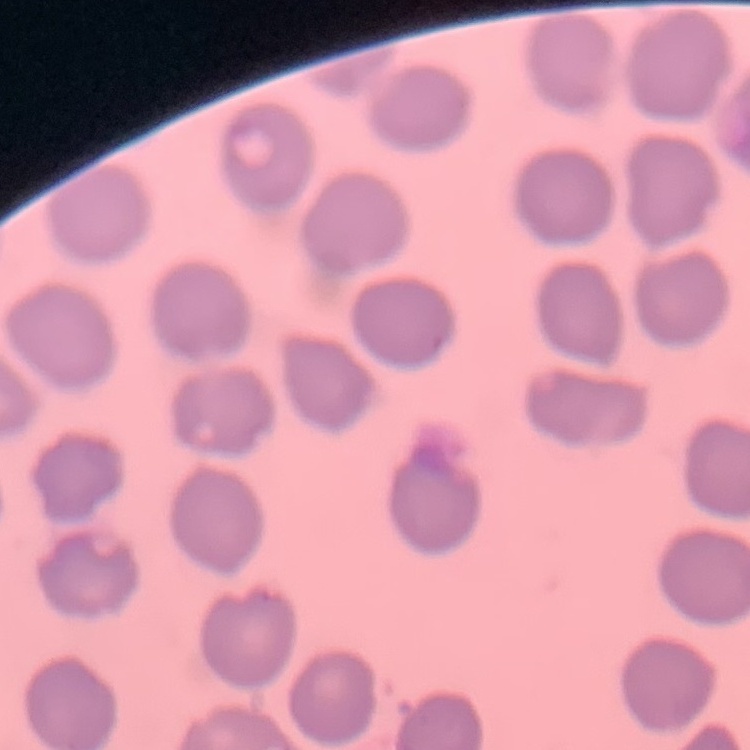

red_blood_cell_morphology: no rouleaux formation
image_type: one tile cut from a larger photomicrograph
stain: Field's or Giemsa
preparation: thin blood film